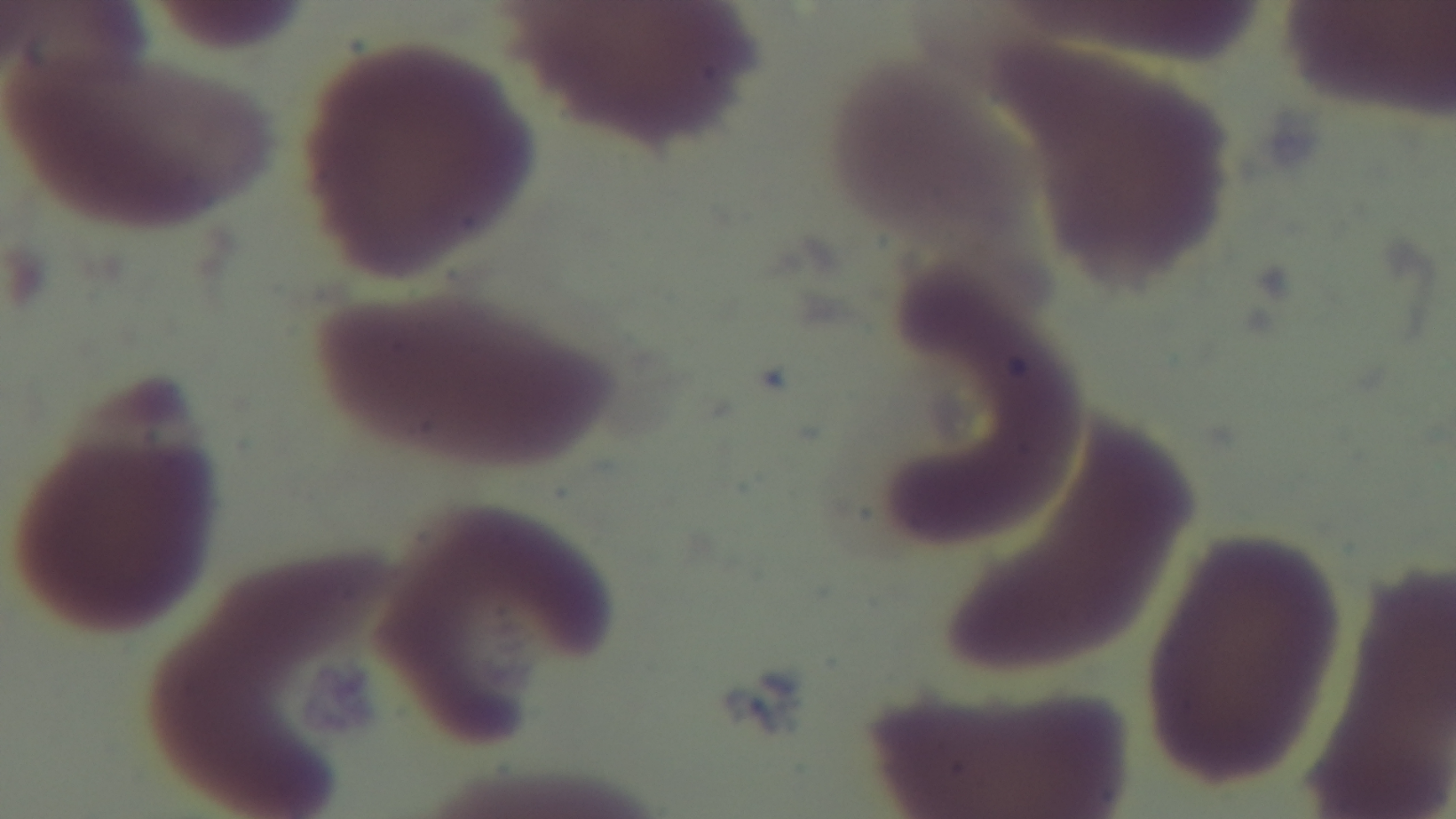
Summary:
  - Stain: Giemsa
  - Malaria status: negative
  - Objective: 100x oil immersion
  - Modality: light microscopy
  - Field of view: one from the slide
  - Preparation: thin smear
  - Capture: mounted 4K digital camera